Assess this cell for malaria.
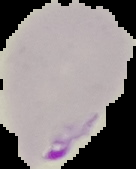

It is parasitized.

{
  "image_size": "136×169 pixels",
  "preparation": "thin blood smear",
  "image_type": "segmented cell region with the area outside set to black"
}